Give the location of every parasitized RBC.
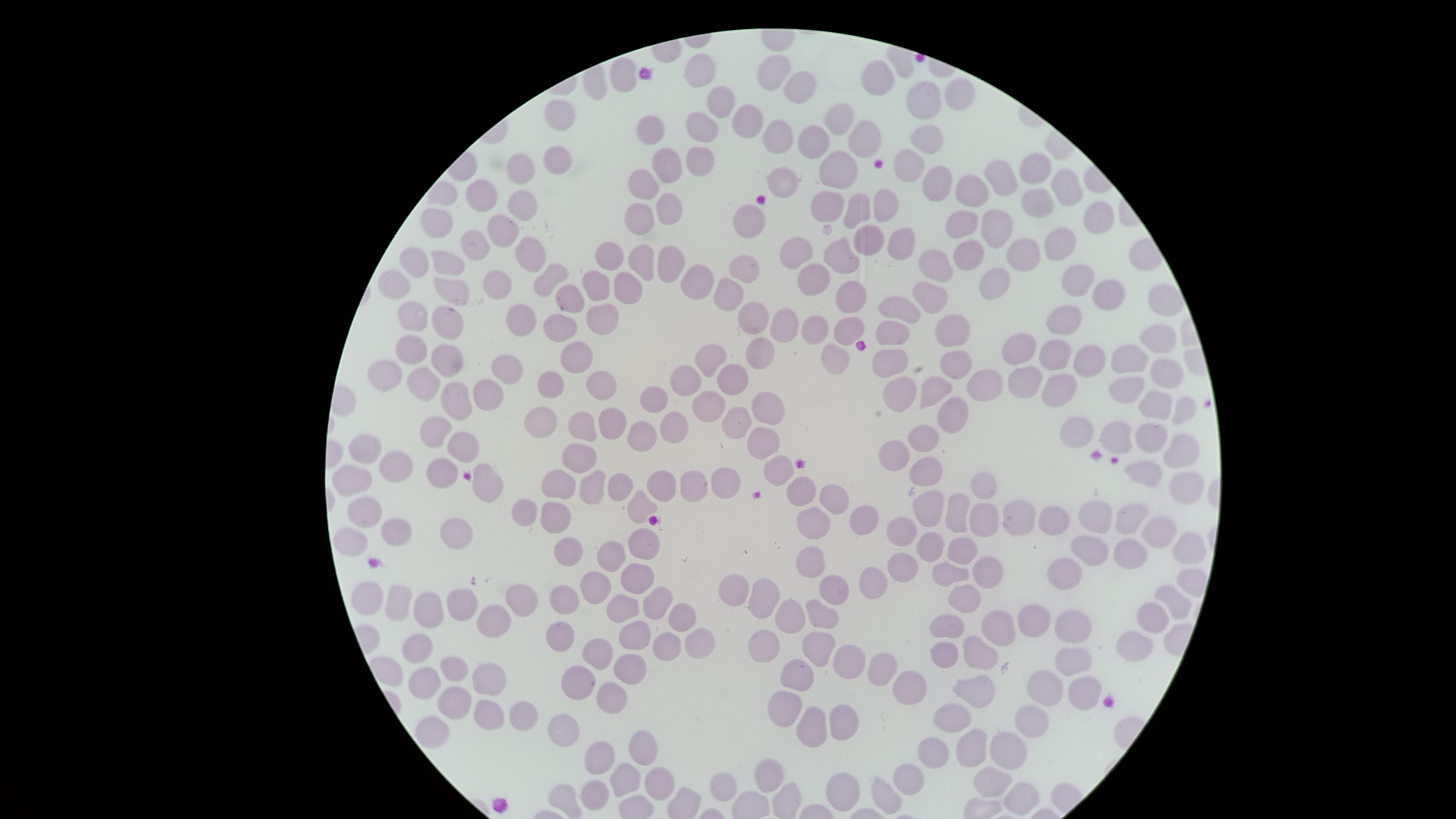
No parasitized RBCs identified.

Approximate marker points as (x, y) in pixels.
Summary:
  - Uninfected RBCs: (700, 72), (781, 73), (622, 75), (880, 75), (799, 92), (959, 96), (924, 101), (726, 104), (564, 117), (840, 117), (749, 121), (698, 125), (651, 128), (778, 136), (924, 136), (865, 139), (813, 142), (701, 157), (554, 159), (672, 161), (839, 164), (906, 168), (523, 171), (1008, 172), (783, 173), (1034, 173), (941, 181), (644, 184), (974, 191), (447, 193), (1063, 193), (483, 196), (831, 202), (1037, 202), (671, 204), (523, 206), (888, 206), (858, 208), (639, 215), (755, 216), (1095, 219), (995, 221), (961, 222), (497, 227), (439, 231), (866, 238), (904, 239), (1053, 244), (474, 247), (797, 248), (527, 253), (969, 254), (1020, 254), (640, 256), (843, 257), (609, 259), (414, 262), (672, 265), (453, 266), (935, 266), (749, 267), (815, 275), (547, 276), (995, 277), (692, 279), (1075, 279), (503, 283), (396, 284), (630, 286), (599, 288), (451, 290), (933, 290), (1109, 293), (730, 296), (851, 297), (1161, 299), (896, 311), (604, 317), (417, 318), (448, 318), (751, 318), (1062, 318), (523, 320), (849, 324), (787, 325), (557, 327), (814, 327), (953, 327), (892, 331), (1158, 334), (1018, 347), (413, 350), (832, 353), (756, 354), (1058, 355), (449, 356), (583, 356), (716, 358), (891, 361), (1084, 361), (1127, 361), (954, 364), (386, 373), (1165, 375), (511, 378), (730, 378), (979, 379), (1022, 380), (682, 382), (1056, 382), (550, 383), (423, 385), (605, 385), (936, 387), (904, 388), (1127, 388), (481, 395), (647, 398), (454, 401), (1160, 401), (708, 404), (770, 404), (1181, 409), (953, 416), (734, 421), (541, 423), (617, 423), (583, 426), (1078, 428), (436, 430), (1119, 431), (634, 433), (670, 433), (927, 435), (1148, 435), (460, 439), (762, 440), (1181, 447), (367, 448), (897, 455), (580, 458), (405, 465), (778, 466), (442, 468), (928, 468), (1145, 472), (353, 475), (487, 482), (725, 482), (1184, 482), (660, 484), (698, 484), (553, 487), (618, 487), (982, 487), (589, 488), (799, 494), (837, 496), (638, 506), (529, 508), (928, 510), (366, 512), (960, 513), (557, 516), (1100, 516), (989, 517), (1017, 517), (1132, 517), (1051, 520), (862, 522), (810, 525), (900, 528), (399, 532), (1155, 534), (458, 537), (641, 542), (346, 543), (1126, 543), (1089, 545), (1187, 545), (570, 547), (924, 548), (960, 552), (608, 555), (809, 559), (906, 562), (1063, 570), (981, 571), (948, 573), (877, 577), (638, 578), (594, 584), (829, 587), (735, 589), (370, 596), (966, 596), (767, 597), (522, 598), (564, 598), (1174, 600), (396, 601), (658, 601), (462, 602), (621, 608), (426, 610), (824, 612), (790, 616), (1036, 616), (1153, 616), (493, 619), (675, 622), (1076, 625), (952, 627), (997, 627), (628, 633), (558, 636), (698, 639), (816, 645), (416, 646), (758, 646), (1131, 646), (663, 647), (980, 647), (944, 652), (594, 653), (842, 658), (1071, 660), (628, 668), (455, 669), (874, 671), (484, 676), (582, 677), (801, 682), (1043, 682), (424, 685), (914, 686), (969, 687), (1085, 689), (612, 695), (455, 701), (520, 709), (789, 711), (483, 713), (947, 714), (844, 720), (1030, 722), (564, 728), (812, 731), (434, 734), (976, 743), (644, 746), (1005, 749), (928, 752), (599, 755), (771, 777), (907, 779), (654, 781), (624, 782), (993, 784), (732, 788), (844, 788), (594, 796), (886, 796), (562, 800), (1021, 801)
  - Stain: Giemsa
  - Capture: smartphone photograph through the microscope eyepiece
  - Field of view: single
  - Preparation: thin smear of blood
  - Visible region: circular
  - Image size: 1456×819 pixels